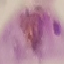

Summary:
  - Malaria status: parasitized
  - Capture: smartphone camera at the microscope eyepiece
  - Stain: Giemsa
  - Image type: cell patch, automatically extracted from a larger field of view and resized to 64 × 64 pixels
  - Preparation: thin blood film